Assess this cell for malaria.
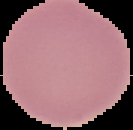

Uninfected.

Summary:
  - Preparation: thin blood film
  - Image size: 133×130 pixels
  - Image type: segmented cell region on a black background